Locate every Plasmodium falciparum-infected red blood cell.
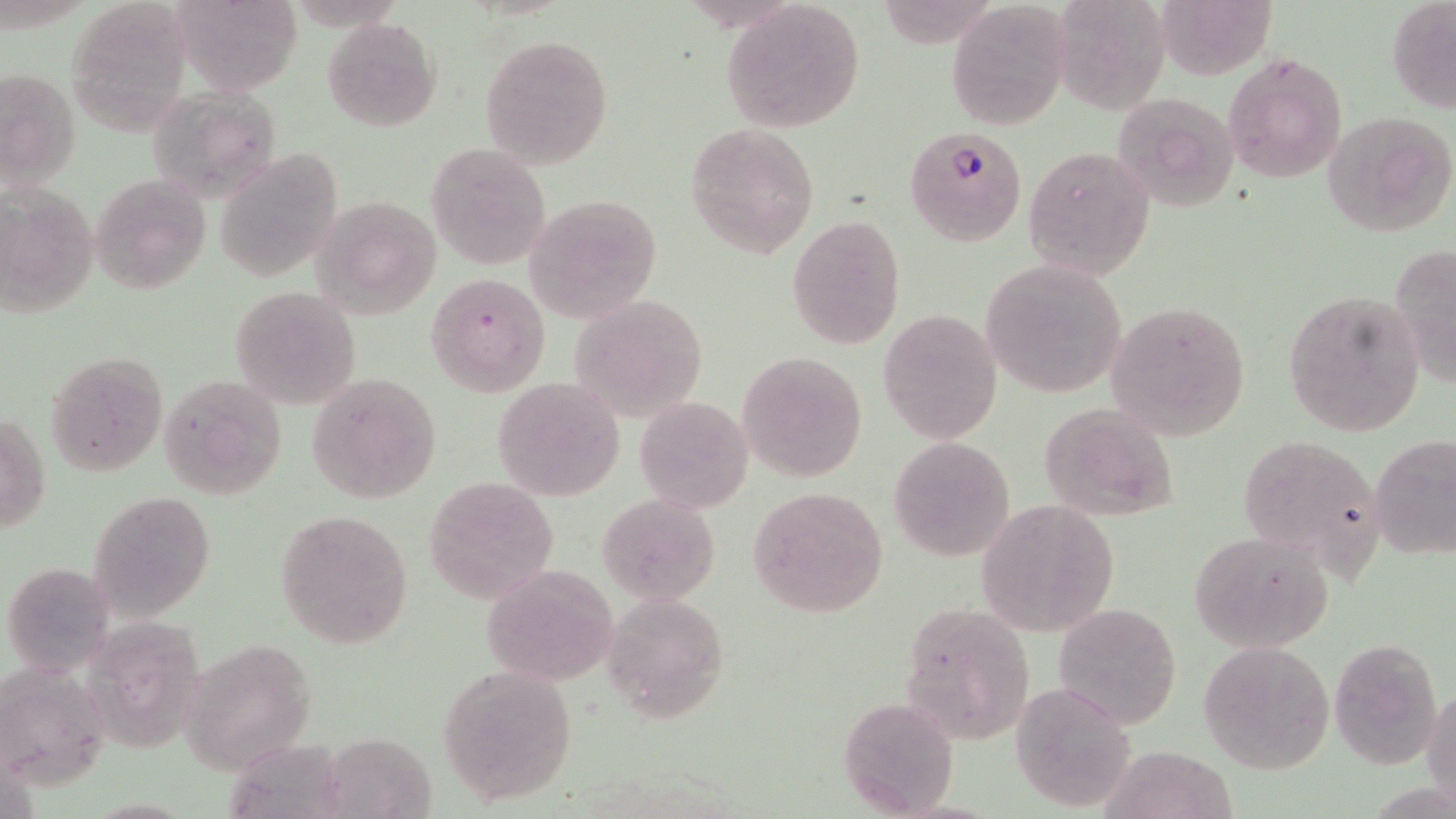

Approximate bounding boxes as named x1/y1/x2/y2 corners in pixels.
Plasmodium falciparum-infected red blood cells: (x1=906, y1=125, x2=1027, y2=246).

slide-level diagnosis = Plasmodium falciparum
field of view = one of a larger specimen
uninfected red blood cell locations = approximate bounding boxes as named x1/y1/x2/y2 corners in pixels: (x1=172, y1=0, x2=302, y2=94), (x1=1052, y1=0, x2=1171, y2=116), (x1=1386, y1=0, x2=1456, y2=113), (x1=720, y1=1, x2=867, y2=132), (x1=948, y1=1, x2=1072, y2=131), (x1=323, y1=17, x2=441, y2=131), (x1=480, y1=34, x2=614, y2=168), (x1=1223, y1=50, x2=1347, y2=185), (x1=0, y1=65, x2=82, y2=193), (x1=143, y1=86, x2=282, y2=202), (x1=1111, y1=91, x2=1243, y2=211), (x1=1321, y1=110, x2=1456, y2=238), (x1=686, y1=123, x2=819, y2=257), (x1=426, y1=144, x2=551, y2=270), (x1=1023, y1=145, x2=1156, y2=280), (x1=214, y1=149, x2=342, y2=281), (x1=90, y1=174, x2=212, y2=294), (x1=526, y1=194, x2=662, y2=322), (x1=311, y1=195, x2=442, y2=319), (x1=787, y1=214, x2=906, y2=349), (x1=1391, y1=243, x2=1456, y2=386), (x1=980, y1=258, x2=1130, y2=400), (x1=427, y1=274, x2=549, y2=395), (x1=230, y1=285, x2=363, y2=410), (x1=1284, y1=287, x2=1427, y2=437), (x1=568, y1=292, x2=708, y2=422), (x1=1105, y1=299, x2=1251, y2=440), (x1=878, y1=309, x2=1002, y2=444), (x1=45, y1=351, x2=169, y2=477), (x1=738, y1=351, x2=868, y2=482), (x1=306, y1=371, x2=441, y2=503), (x1=161, y1=372, x2=289, y2=500), (x1=492, y1=377, x2=624, y2=501), (x1=635, y1=396, x2=755, y2=515), (x1=1039, y1=402, x2=1180, y2=521), (x1=1, y1=409, x2=49, y2=536), (x1=1235, y1=432, x2=1386, y2=570), (x1=1372, y1=432, x2=1456, y2=560), (x1=888, y1=436, x2=1015, y2=562), (x1=423, y1=477, x2=557, y2=602), (x1=747, y1=486, x2=888, y2=617), (x1=87, y1=489, x2=217, y2=621), (x1=597, y1=491, x2=721, y2=607), (x1=974, y1=500, x2=1119, y2=636), (x1=277, y1=508, x2=413, y2=651), (x1=1190, y1=530, x2=1334, y2=652), (x1=3, y1=561, x2=116, y2=677), (x1=482, y1=564, x2=621, y2=686), (x1=601, y1=591, x2=730, y2=722), (x1=86, y1=598, x2=209, y2=756), (x1=897, y1=601, x2=1035, y2=745), (x1=1053, y1=602, x2=1181, y2=729), (x1=1329, y1=635, x2=1445, y2=768), (x1=179, y1=636, x2=318, y2=775), (x1=1197, y1=641, x2=1334, y2=774), (x1=3, y1=662, x2=112, y2=790), (x1=436, y1=666, x2=579, y2=807), (x1=1012, y1=680, x2=1138, y2=812), (x1=1424, y1=685, x2=1456, y2=805), (x1=837, y1=693, x2=962, y2=818)
magnification = 1000x
image size = 1456×819 pixels
modality = optical microscopy
preparation = thin blood film
stain = May-Grünwald-Giemsa